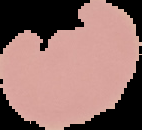
Image is 142×130 pixels. Segmented cell region on a black background. Result: negative for Plasmodium parasites. From a thin blood film.